Locate every Plasmodium parasite.
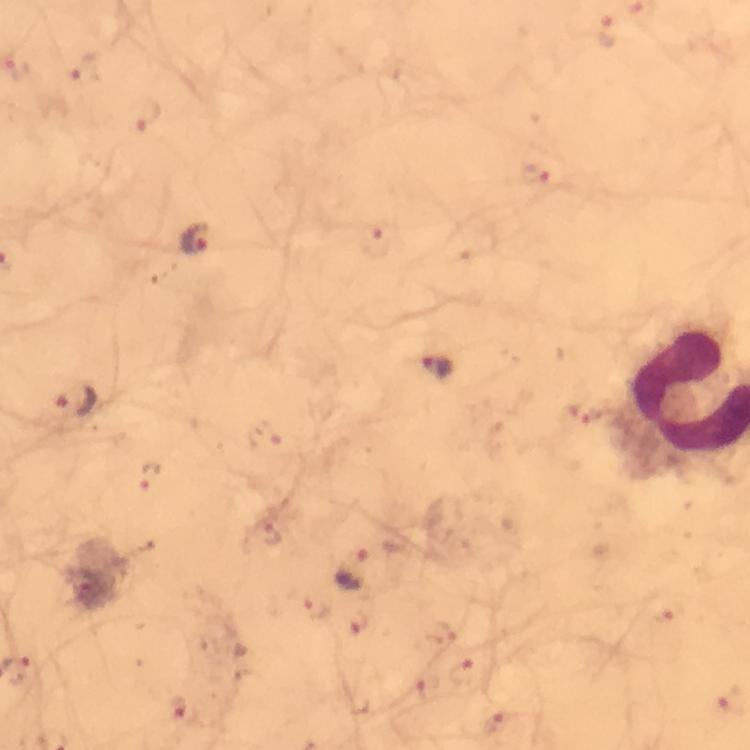

Approximate object centers, in pixels from the top-left corner.
Plasmodium parasites: (x=609, y=33), (x=85, y=67), (x=149, y=117), (x=536, y=177), (x=195, y=239), (x=379, y=242), (x=76, y=405), (x=265, y=438), (x=152, y=477), (x=268, y=537), (x=355, y=568), (x=311, y=606), (x=660, y=613), (x=361, y=627), (x=444, y=635), (x=463, y=671), (x=427, y=688), (x=178, y=707), (x=495, y=726).

Summary:
  - Magnification: 100x
  - Cropped from: a single field of view
  - Stain: Giemsa
  - Preparation: thick blood film
  - Context: from a malaria diagnostic workup
  - Image size: 750×750 pixels
  - Capture: smartphone camera through the microscope
  - Immersion oil: used